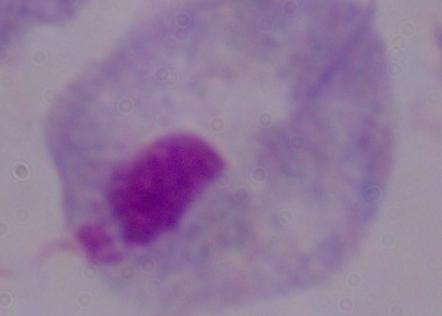

Summary:
  - Identification: trichomonad
  - Magnification: 1000x
  - Modality: photomicrograph